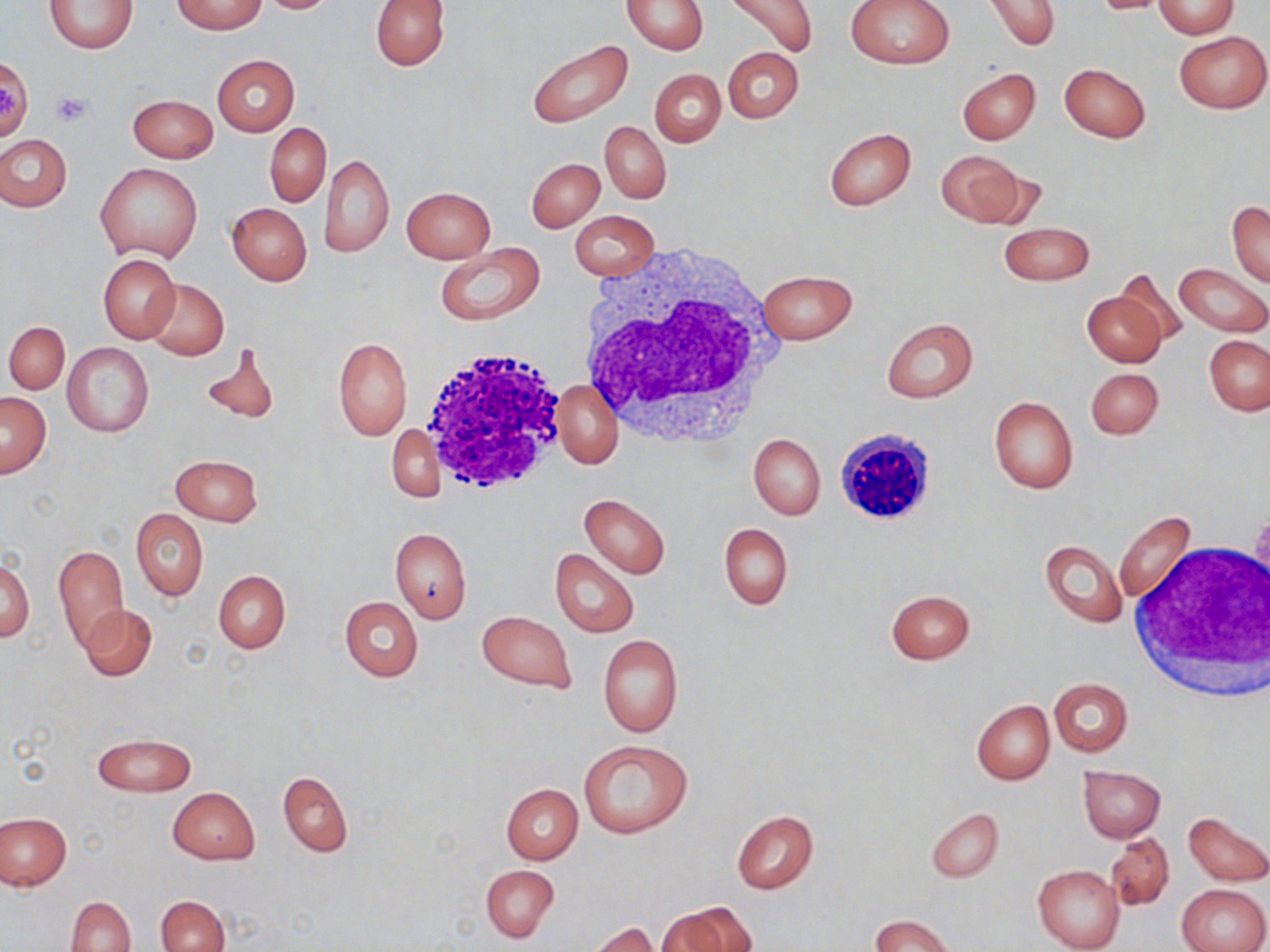
slide-level diagnosis = negative for blood parasites
field of view = one of a larger specimen
platelet locations = approximate bounding boxes as named x1/y1/x2/y2 corners in pixels: (x1=51, y1=91, x2=93, y2=127)
uninfected red blood cell locations = approximate bounding boxes as named x1/y1/x2/y2 corners in pixels: (x1=44, y1=0, x2=137, y2=54), (x1=174, y1=0, x2=265, y2=34), (x1=256, y1=0, x2=339, y2=13), (x1=370, y1=0, x2=449, y2=70), (x1=722, y1=0, x2=817, y2=58), (x1=846, y1=0, x2=954, y2=69), (x1=985, y1=0, x2=1059, y2=49), (x1=1089, y1=0, x2=1174, y2=15), (x1=1153, y1=0, x2=1239, y2=38), (x1=621, y1=1, x2=707, y2=54), (x1=1174, y1=31, x2=1268, y2=113), (x1=527, y1=38, x2=633, y2=128), (x1=723, y1=47, x2=804, y2=123), (x1=212, y1=54, x2=300, y2=135), (x1=1058, y1=62, x2=1151, y2=143), (x1=957, y1=67, x2=1041, y2=144), (x1=650, y1=69, x2=726, y2=147), (x1=128, y1=93, x2=218, y2=162), (x1=600, y1=121, x2=670, y2=203), (x1=266, y1=122, x2=330, y2=205), (x1=824, y1=127, x2=915, y2=211), (x1=0, y1=133, x2=72, y2=211), (x1=935, y1=150, x2=1028, y2=227), (x1=320, y1=154, x2=393, y2=259), (x1=528, y1=158, x2=605, y2=232), (x1=95, y1=163, x2=204, y2=263), (x1=400, y1=186, x2=495, y2=264), (x1=412, y1=191, x2=522, y2=306), (x1=1227, y1=201, x2=1270, y2=287), (x1=227, y1=203, x2=311, y2=285), (x1=571, y1=211, x2=660, y2=281), (x1=1000, y1=221, x2=1094, y2=287), (x1=434, y1=245, x2=545, y2=325), (x1=98, y1=254, x2=181, y2=344), (x1=1174, y1=262, x2=1270, y2=338), (x1=757, y1=268, x2=858, y2=345), (x1=1114, y1=268, x2=1189, y2=350), (x1=145, y1=279, x2=228, y2=358), (x1=1083, y1=291, x2=1167, y2=367), (x1=880, y1=316, x2=978, y2=403), (x1=4, y1=320, x2=70, y2=395), (x1=334, y1=336, x2=413, y2=441), (x1=1203, y1=336, x2=1270, y2=416), (x1=198, y1=341, x2=279, y2=425), (x1=63, y1=342, x2=154, y2=438), (x1=1085, y1=367, x2=1164, y2=440), (x1=554, y1=379, x2=624, y2=469), (x1=1, y1=392, x2=52, y2=478), (x1=988, y1=395, x2=1079, y2=493), (x1=385, y1=425, x2=445, y2=502), (x1=748, y1=433, x2=825, y2=520), (x1=171, y1=453, x2=262, y2=526), (x1=580, y1=494, x2=670, y2=579), (x1=131, y1=508, x2=208, y2=601), (x1=1114, y1=511, x2=1197, y2=607), (x1=719, y1=523, x2=792, y2=608), (x1=389, y1=527, x2=472, y2=623), (x1=1040, y1=539, x2=1127, y2=628), (x1=53, y1=544, x2=129, y2=650), (x1=550, y1=548, x2=639, y2=637), (x1=1, y1=559, x2=33, y2=642), (x1=213, y1=570, x2=290, y2=653), (x1=886, y1=589, x2=975, y2=663), (x1=340, y1=596, x2=422, y2=681), (x1=79, y1=603, x2=157, y2=681), (x1=477, y1=610, x2=577, y2=692), (x1=598, y1=634, x2=683, y2=737), (x1=1048, y1=677, x2=1132, y2=757), (x1=972, y1=700, x2=1054, y2=784), (x1=92, y1=733, x2=197, y2=796), (x1=578, y1=739, x2=693, y2=839), (x1=1078, y1=765, x2=1166, y2=842), (x1=277, y1=771, x2=352, y2=856), (x1=503, y1=783, x2=582, y2=864), (x1=168, y1=787, x2=260, y2=863), (x1=926, y1=808, x2=1003, y2=881), (x1=731, y1=810, x2=818, y2=894), (x1=0, y1=812, x2=71, y2=889), (x1=1182, y1=812, x2=1270, y2=886), (x1=1106, y1=832, x2=1174, y2=911), (x1=480, y1=864, x2=559, y2=942), (x1=1032, y1=864, x2=1124, y2=952), (x1=1178, y1=882, x2=1269, y2=952), (x1=156, y1=894, x2=230, y2=952), (x1=67, y1=895, x2=135, y2=952), (x1=660, y1=902, x2=758, y2=952), (x1=870, y1=914, x2=957, y2=952), (x1=588, y1=922, x2=659, y2=951)
magnification = 1000x
modality = light microscopy
image size = 1270×952 pixels
white blood cell locations = approximate bounding boxes as named x1/y1/x2/y2 corners in pixels: (x1=576, y1=243, x2=782, y2=448), (x1=416, y1=348, x2=569, y2=495), (x1=839, y1=425, x2=939, y2=527), (x1=1126, y1=540, x2=1269, y2=700)
stain = May-Grünwald-Giemsa
preparation = thin blood smear